Assess this cell for malaria.
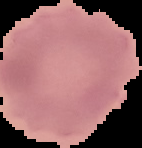
It is uninfected.

From a thin blood film. Image is 142×148 pixels. Cell region segmented out of the field of view; the surrounding area is masked to black.